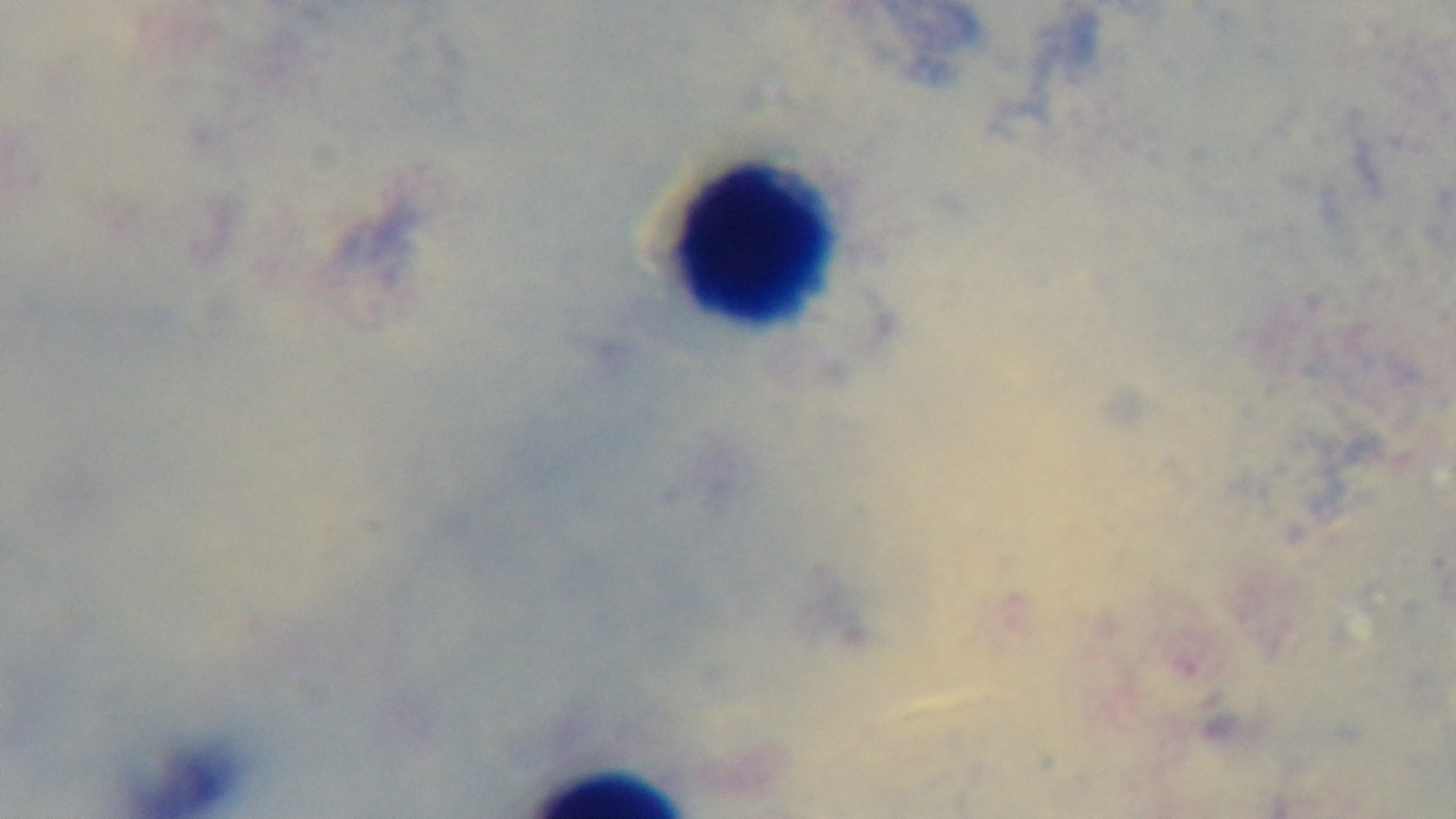

Summary:
  - Preparation: thick blood film
  - Objective: 100x oil immersion
  - Field of view: one from the slide
  - Stain: Giemsa
  - Capture: mounted 4K digital camera
  - Modality: light microscopy
  - Malaria status: uninfected